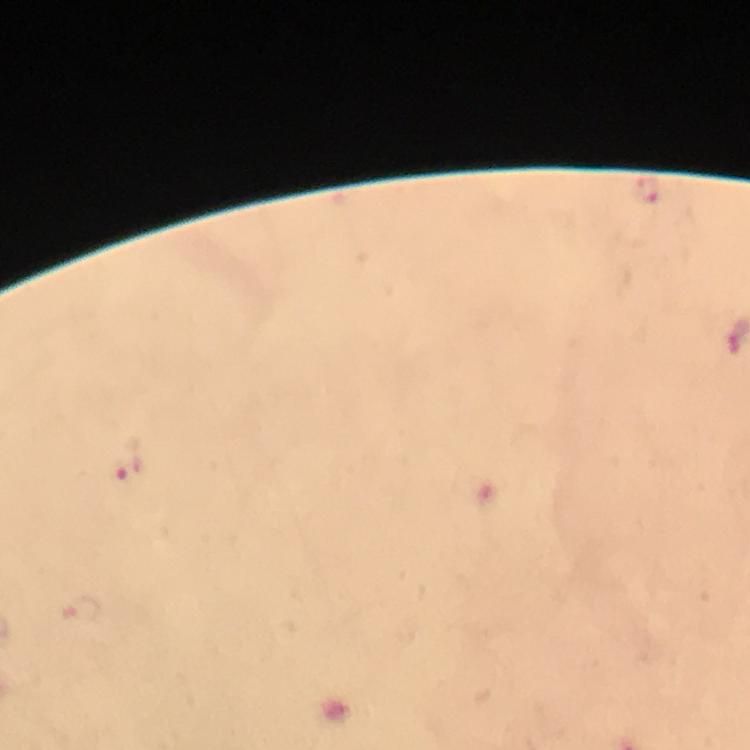

Approximate object centers, in pixels from the top-left corner.
Summary:
  - Plasmodium parasite locations: (x=646, y=191), (x=127, y=469)
  - Context: from a diagnostic examination for malaria
  - Capture: smartphone camera through the microscope
  - Cropped from: a single field of view
  - Stain: Giemsa
  - Image size: 750×750 pixels
  - Immersion oil: applied
  - Magnification: 100x
  - Preparation: thick blood film